Assess this cell for malaria.
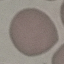
Uninfected.

Acquired by smartphone through the microscope eyepiece. Cell patch, automatically extracted from a larger field of view and resized to 64 × 64 pixels. Giemsa-stained preparation. Thin blood film.